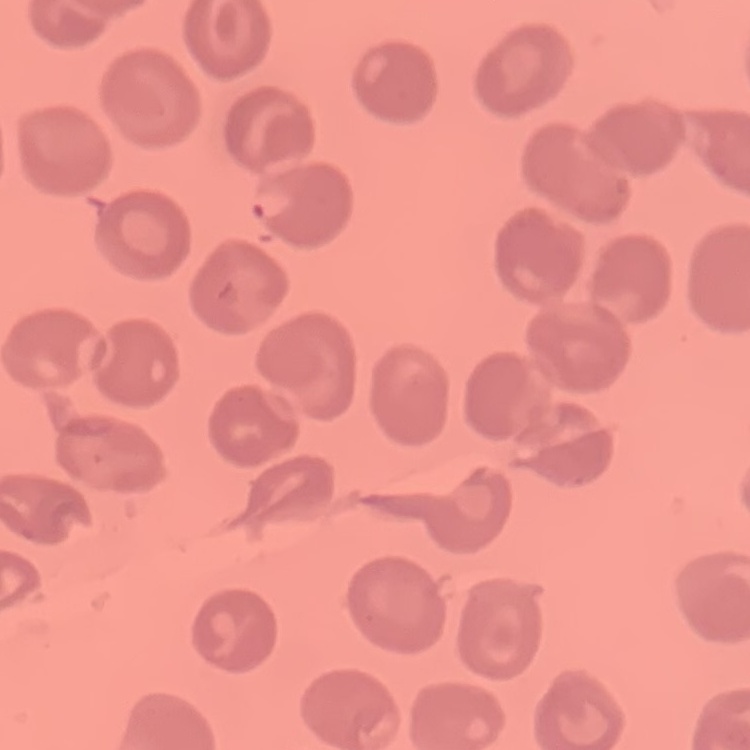
red_blood_cell_morphology: no rouleaux formation
image_type: one tile cut from a larger photomicrograph
stain: Field's or Giemsa
preparation: thin blood smear